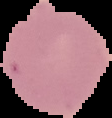 Malaria status: uninfected. From a thin blood smear. Image is 112×118 pixels. Segmented cell region on a black background.